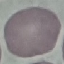
{
  "malaria_status": "uninfected",
  "stain": "Giemsa",
  "preparation": "thin blood film",
  "image_type": "automatically extracted cell patch, resized to 64 × 64 pixels",
  "capture": "smartphone through the microscope eyepiece"
}